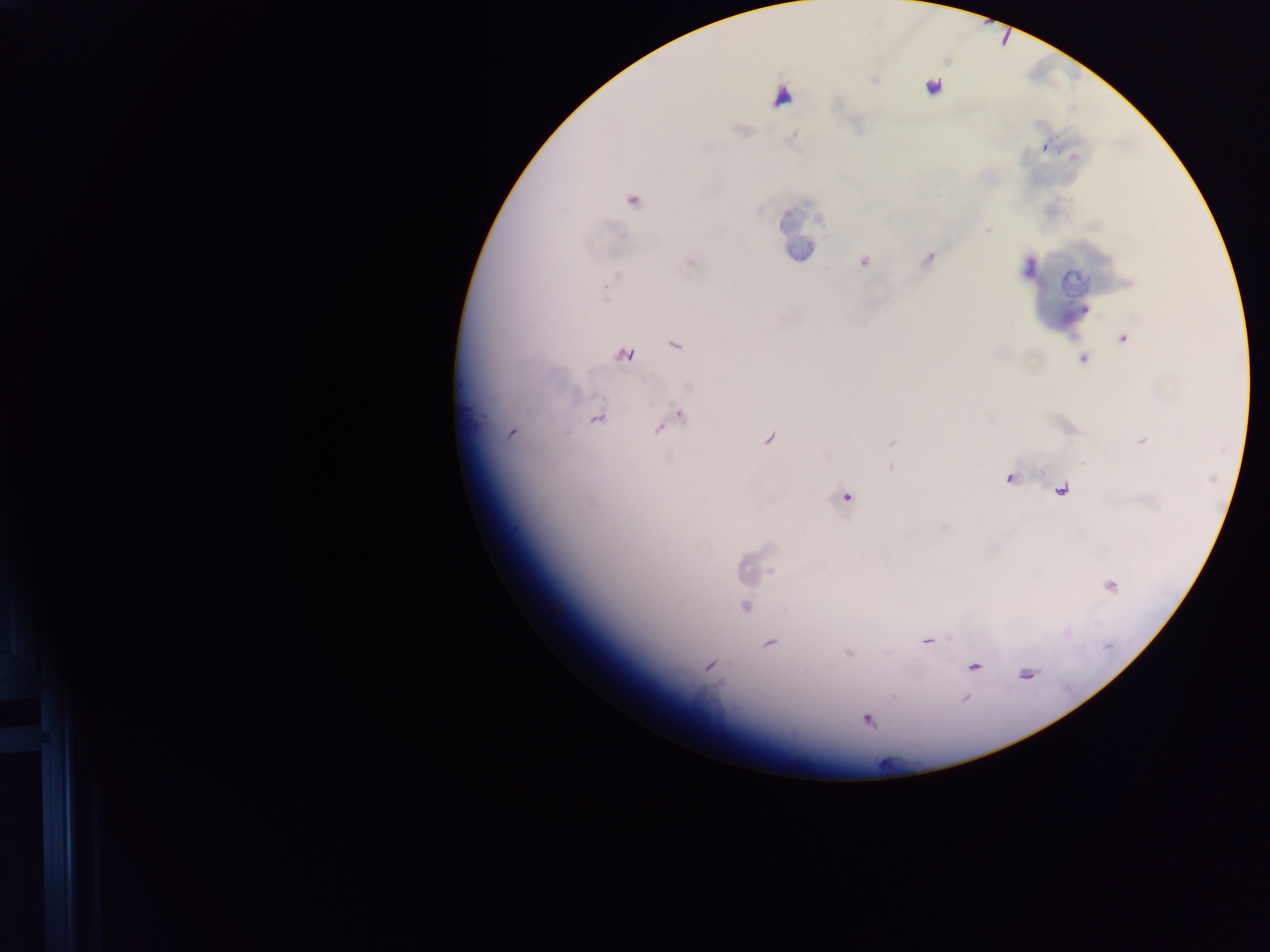
leukocyte locations = approximate centers as x y in pixels: 934 85; 783 96; 806 230; 1076 283
country = Ghana
field of view = single
capture = mobile-phone photograph through a microscope
malaria parasite locations = approximate centers as x y in pixels: 1045 147; 929 258; 863 262; 606 289; 1084 310; 1124 337; 675 345; 623 356; 1082 359; 680 416; 597 419; 511 434; 769 439; 892 443; 891 466; 1009 478; 1061 488; 846 498; 745 607; 926 642; 769 643; 848 653; 708 666; 973 667; 1027 675; 893 698; 965 699; 867 720
image size = 1270×952 pixels
preparation = thick blood smear